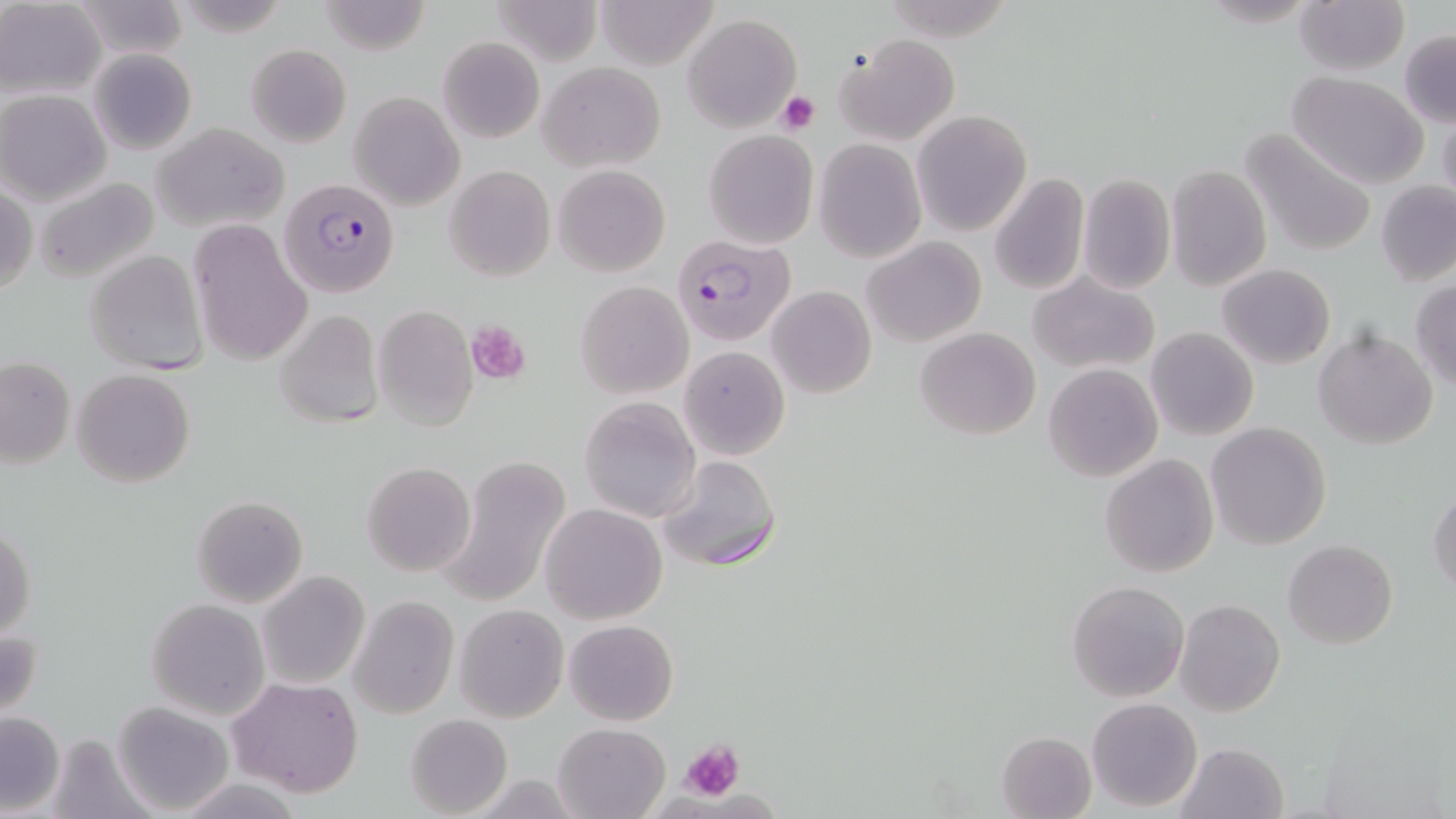 Approximate bounding boxes as (x1, y1, x2, y2) in pixels. Platelet locations: (775, 90, 820, 134), (466, 321, 531, 384), (682, 738, 745, 801). Uninfected red blood cell locations: (488, 0, 603, 66), (593, 0, 721, 69), (1, 1, 105, 99), (70, 1, 192, 61), (317, 1, 431, 55), (1294, 1, 1408, 75), (682, 14, 802, 132), (1400, 31, 1456, 126), (835, 33, 961, 146), (436, 36, 544, 144), (243, 43, 352, 148), (87, 48, 198, 155), (537, 62, 666, 172), (1286, 72, 1429, 190), (1, 90, 114, 207), (349, 92, 465, 211), (1438, 107, 1456, 215), (911, 111, 1031, 236), (153, 121, 291, 232), (1239, 126, 1379, 258), (703, 130, 818, 248), (813, 140, 926, 262), (552, 164, 671, 277), (1166, 165, 1271, 290), (443, 166, 555, 281), (1076, 172, 1176, 294), (990, 175, 1090, 297), (33, 178, 161, 286), (1376, 181, 1455, 286), (1, 183, 37, 296), (186, 221, 313, 367), (862, 236, 986, 347), (86, 249, 207, 374), (1217, 263, 1336, 369), (1030, 272, 1160, 374), (577, 281, 693, 399), (1409, 281, 1456, 391), (767, 286, 876, 398), (373, 305, 479, 431), (272, 308, 386, 430), (715, 308, 868, 424), (914, 327, 1042, 440), (1145, 327, 1259, 442), (1314, 328, 1439, 448), (678, 345, 790, 460), (1, 357, 75, 469), (1043, 364, 1163, 482), (71, 367, 197, 489), (578, 395, 702, 523), (1205, 422, 1333, 550), (437, 454, 572, 609), (1100, 454, 1219, 577), (656, 455, 780, 573), (361, 462, 476, 576), (1428, 489, 1456, 598), (191, 494, 308, 608), (540, 503, 668, 624), (0, 523, 36, 640), (1284, 540, 1398, 649), (257, 571, 369, 690), (1066, 579, 1188, 703), (348, 595, 459, 719), (145, 599, 270, 718), (1175, 599, 1284, 716), (454, 604, 569, 722), (563, 619, 679, 727), (0, 623, 44, 726), (228, 677, 365, 798), (1087, 698, 1203, 813), (113, 702, 235, 816), (0, 709, 65, 816), (405, 713, 513, 818), (552, 721, 672, 818), (43, 731, 152, 818), (997, 731, 1097, 819), (1174, 741, 1289, 819), (463, 774, 591, 816). Plasmodium falciparum-infected red blood cell locations: (279, 176, 400, 297), (673, 234, 797, 345). Slide-level diagnosis: Plasmodium falciparum. Captured at 1000x magnification. Image is 1456×819 pixels. Thin blood smear. One field of a larger specimen. Optical microscopy. May-Grünwald-Giemsa stain.